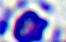

{
  "modality": "micrograph",
  "magnification": "400x",
  "identification": "white blood cell"
}